Assess this cell for malaria.
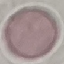
It is uninfected.

Thin smear of blood. Giemsa stain. Photographed with a smartphone camera at the microscope eyepiece. Cell patch, automatically extracted from a larger field of view and resized to 64 × 64 pixels.